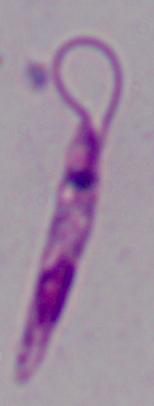

Summary:
  - Identification: Leishmania
  - Magnification: 1000x
  - Modality: micrograph